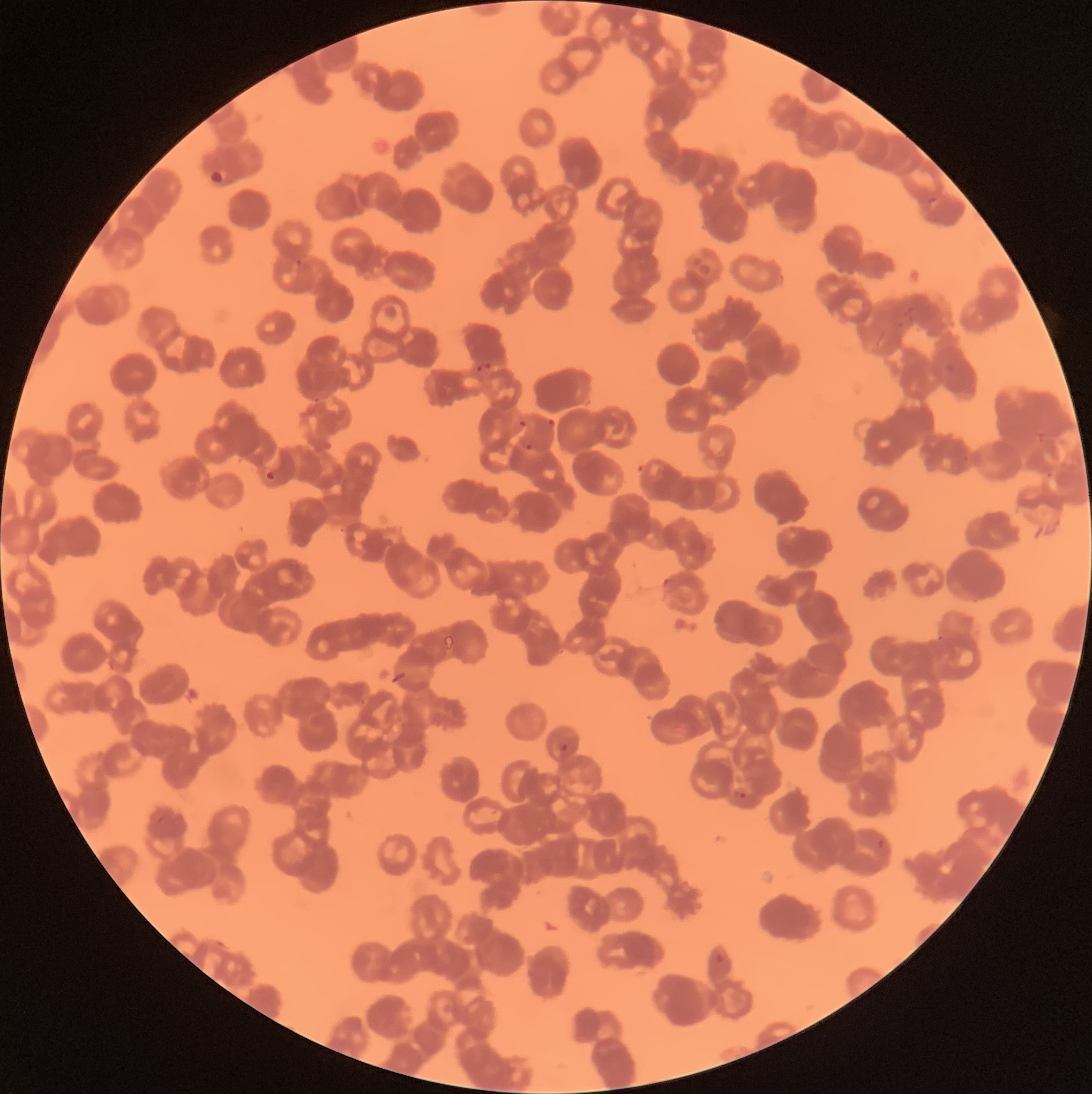

Summary:
  - Coordinate format: approximate bounding boxes as (x1,y1)-(x2,y2) corner pairs in pixels
  - Plasmodium parasite locations: (295,258)-(303,266), (661,577)-(669,589), (559,743)-(570,751), (736,791)-(750,801), (156,816)-(164,824), (875,835)-(891,857)
  - Modality: optical microscopy
  - Preparation: thin blood smear
  - Image size: 1092×1094 pixels
  - Red blood cell morphology: rouleaux formation